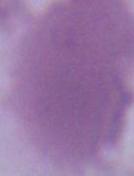
Micrograph. Captured at 1000x magnification. An erythrocyte is shown.